Assess this cell for malaria.
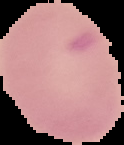
It is uninfected.

From a thin blood film. Image is 124×145 pixels. The area outside the segmented cell region is set to black.